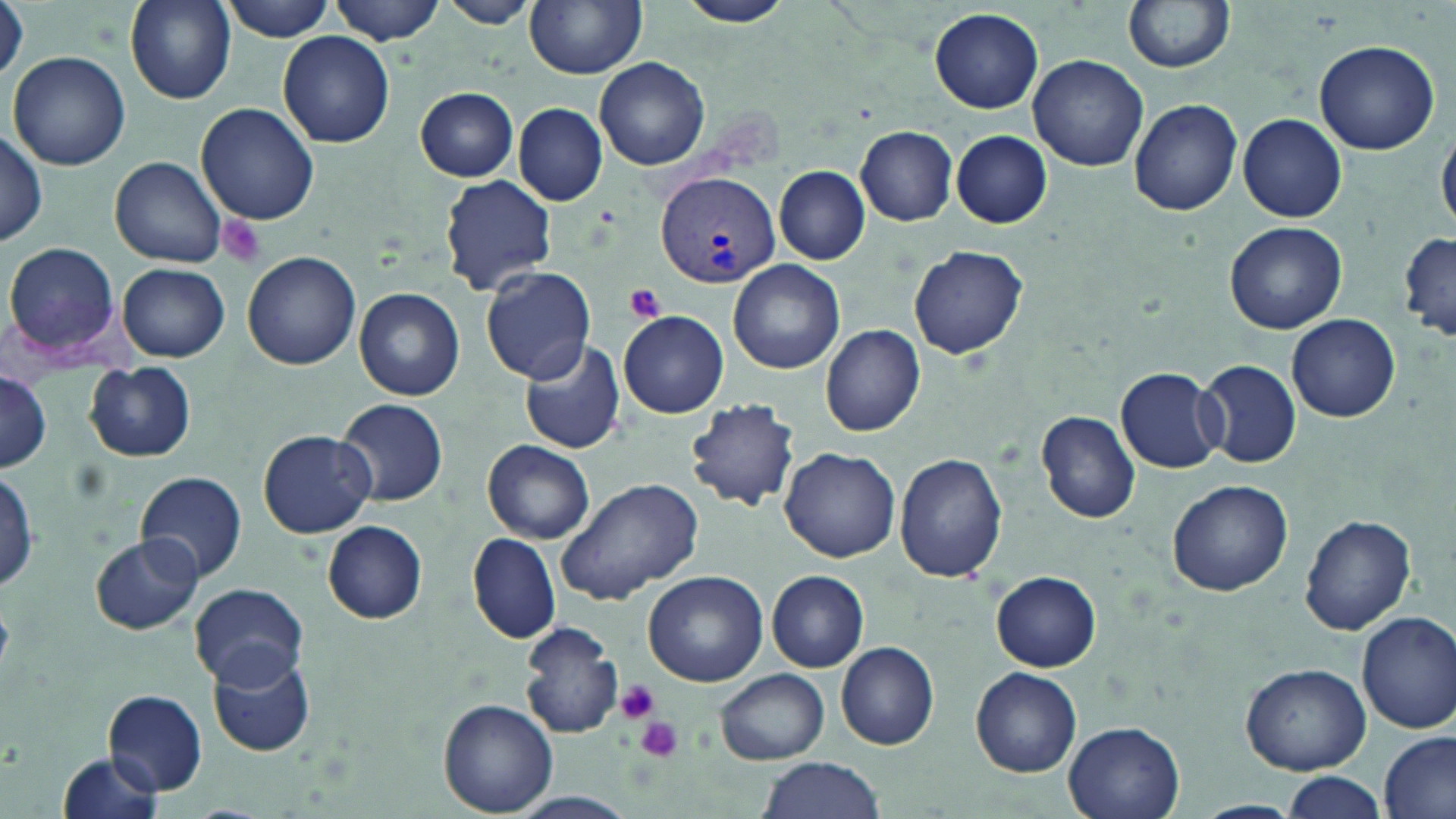

Summary:
  - Coordinate format: approximate bounding boxes as (x1, y1, x2, y2) in pixels
  - Plasmodium vivax-infected red blood cell locations: (656, 174, 781, 288)
  - Platelet locations: (216, 215, 265, 267), (624, 283, 666, 325), (614, 679, 663, 724), (635, 717, 684, 764)
  - Uninfected red blood cell locations: (123, 0, 238, 106), (218, 0, 338, 41), (332, 0, 445, 44), (441, 0, 537, 28), (526, 0, 648, 77), (676, 0, 795, 27), (1122, 0, 1235, 74), (929, 7, 1044, 114), (277, 32, 395, 147), (1314, 37, 1441, 154), (7, 51, 130, 170), (1027, 54, 1148, 172), (593, 57, 709, 171), (415, 88, 519, 180), (1129, 97, 1243, 215), (514, 102, 607, 205), (197, 103, 322, 226), (1239, 113, 1346, 222), (0, 124, 49, 248), (1437, 125, 1456, 235), (856, 126, 957, 225), (951, 131, 1052, 228), (112, 157, 228, 268), (775, 166, 870, 265), (440, 176, 556, 295), (1224, 221, 1347, 334), (1398, 233, 1456, 343), (5, 242, 122, 359), (909, 244, 1029, 359), (242, 251, 362, 370), (729, 259, 846, 374), (119, 263, 230, 360), (481, 266, 595, 383), (354, 288, 465, 399), (619, 311, 730, 418), (1285, 315, 1401, 423), (822, 325, 925, 436), (517, 338, 627, 456), (1198, 359, 1302, 468), (84, 363, 196, 462), (1117, 368, 1226, 472), (0, 372, 53, 473), (338, 397, 448, 506), (686, 400, 802, 512), (1036, 411, 1140, 525), (258, 429, 376, 538), (483, 440, 595, 543), (780, 448, 900, 563), (476, 451, 578, 650), (893, 453, 1008, 584), (0, 467, 38, 595), (134, 471, 248, 583), (556, 476, 704, 606), (1167, 479, 1294, 597), (1298, 514, 1416, 638), (321, 520, 428, 623), (91, 532, 202, 636), (468, 533, 561, 643), (642, 570, 768, 685), (767, 571, 870, 671), (992, 572, 1102, 671), (189, 582, 309, 689), (1356, 612, 1456, 731), (519, 621, 622, 739), (835, 642, 940, 749), (206, 647, 316, 757), (1241, 663, 1371, 774), (717, 667, 830, 764), (971, 668, 1081, 777), (103, 689, 210, 797), (438, 699, 559, 817), (1063, 720, 1186, 819), (1381, 731, 1456, 818), (55, 751, 168, 819), (754, 757, 885, 819), (1282, 772, 1382, 819), (512, 791, 636, 817), (1192, 800, 1304, 819)
  - Slide-level diagnosis: Plasmodium vivax
  - Magnification: 1000x
  - Image size: 1456×819 pixels
  - Stain: May-Grünwald-Giemsa
  - Field of view: one of a larger specimen
  - Preparation: thin blood smear
  - Modality: light microscopy